Outline platelets.
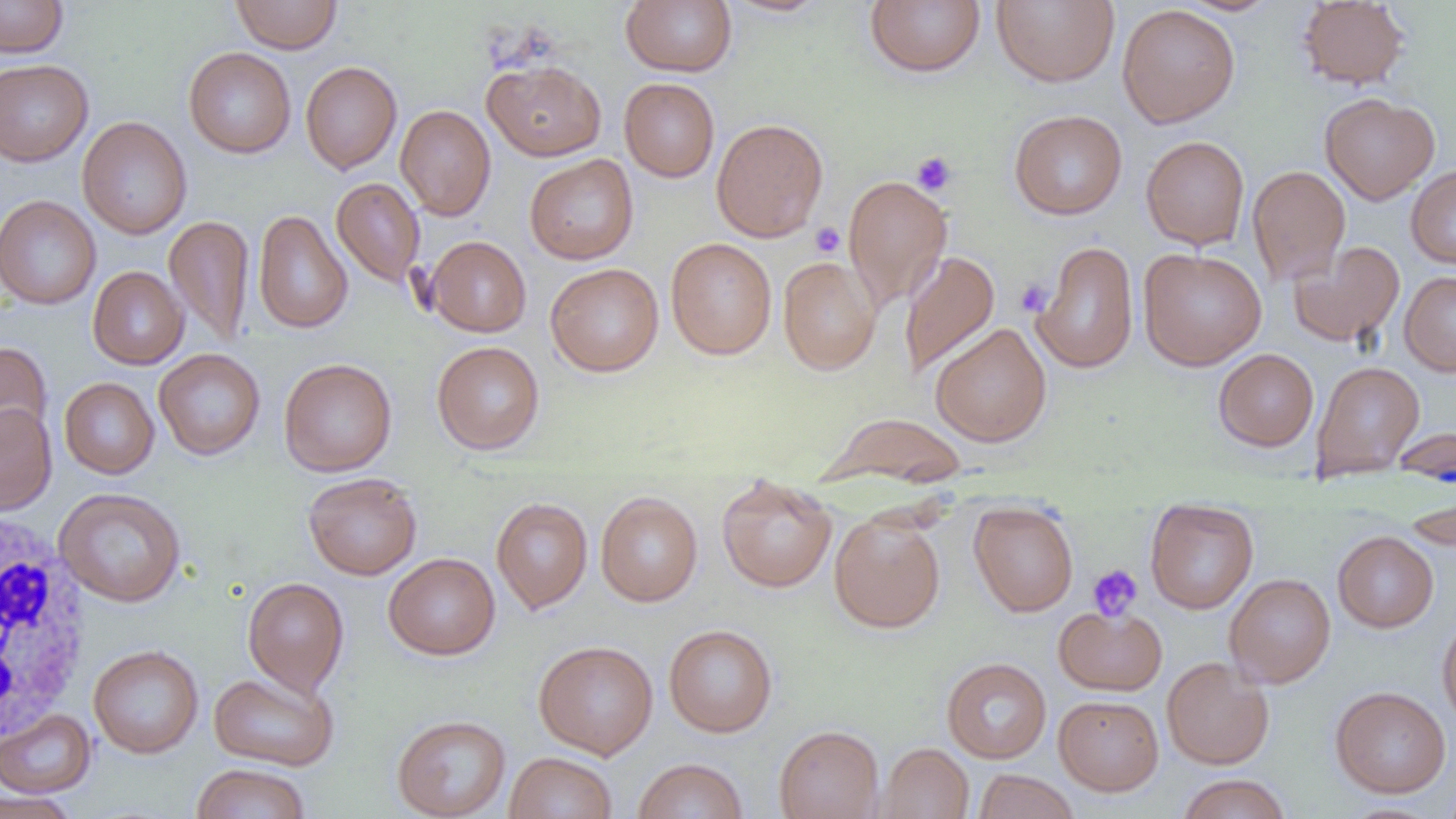
Approximate bounding boxes as (x1, y1, x2, y2) in pixels.
Platelets: (911, 151, 957, 196), (810, 222, 845, 258), (1015, 279, 1053, 316), (1088, 564, 1143, 621).

slide-level diagnosis = no evidence of blood parasites
field of view = one of a larger specimen
magnification = 1000x
preparation = thin blood film
uninfected red blood cell locations (subset) = approximate bounding boxes as (x1, y1, x2, y2) in pixels: (0, 0, 69, 58), (231, 0, 342, 54), (620, 0, 737, 76), (722, 0, 833, 17), (865, 0, 986, 77), (992, 0, 1119, 87), (1177, 0, 1283, 16), (1296, 1, 1411, 90), (1117, 3, 1240, 128), (183, 47, 296, 158), (483, 58, 606, 161), (0, 59, 93, 166), (300, 61, 402, 174), (619, 78, 719, 182), (1319, 92, 1439, 204), (395, 104, 496, 220), (1009, 109, 1127, 220), (77, 116, 193, 240), (711, 118, 828, 243), (1141, 135, 1249, 249), (524, 154, 639, 265), (1247, 165, 1350, 286), (1406, 165, 1456, 269), (843, 174, 952, 311), (331, 177, 425, 288), (0, 194, 101, 310), (253, 209, 353, 334), (164, 215, 255, 346), (426, 235, 531, 337), (666, 238, 777, 360), (1031, 240, 1139, 374), (1288, 241, 1405, 348), (1138, 248, 1267, 371), (899, 249, 1001, 380), (778, 255, 881, 375), (545, 263, 664, 377), (87, 266, 189, 370), (1399, 271, 1456, 376), (930, 322, 1052, 447), (431, 340, 545, 455), (0, 341, 53, 449), (153, 348, 266, 460), (1213, 348, 1319, 451), (278, 357, 397, 477), (1310, 360, 1426, 480), (59, 377, 159, 479), (0, 403, 57, 515), (824, 412, 968, 487), (1393, 425, 1456, 489), (303, 472, 422, 580), (716, 476, 838, 593), (1405, 482, 1456, 554), (595, 490, 703, 607), (491, 497, 593, 613), (1145, 499, 1259, 615), (969, 502, 1078, 616), (829, 511, 946, 634), (1333, 531, 1439, 632), (383, 552, 500, 660), (1224, 573, 1336, 688), (242, 576, 349, 696), (1054, 605, 1167, 696), (1437, 615, 1456, 731), (664, 624, 777, 737), (533, 640, 658, 759), (88, 645, 204, 758), (1162, 656, 1274, 769), (941, 657, 1052, 763), (208, 670, 339, 771), (1330, 686, 1451, 798), (1053, 695, 1164, 796), (0, 710, 96, 798), (392, 714, 511, 818), (774, 725, 884, 819), (876, 743, 974, 819), (505, 752, 617, 819), (632, 757, 748, 819), (190, 763, 311, 819), (972, 769, 1079, 819), (1177, 774, 1292, 818), (0, 790, 79, 819)
image size = 1456×819 pixels
modality = light microscopy
white blood cell locations (subset) = approximate bounding boxes as (x1, y1, x2, y2) in pixels: (1, 512, 91, 746)